State the preparation type.
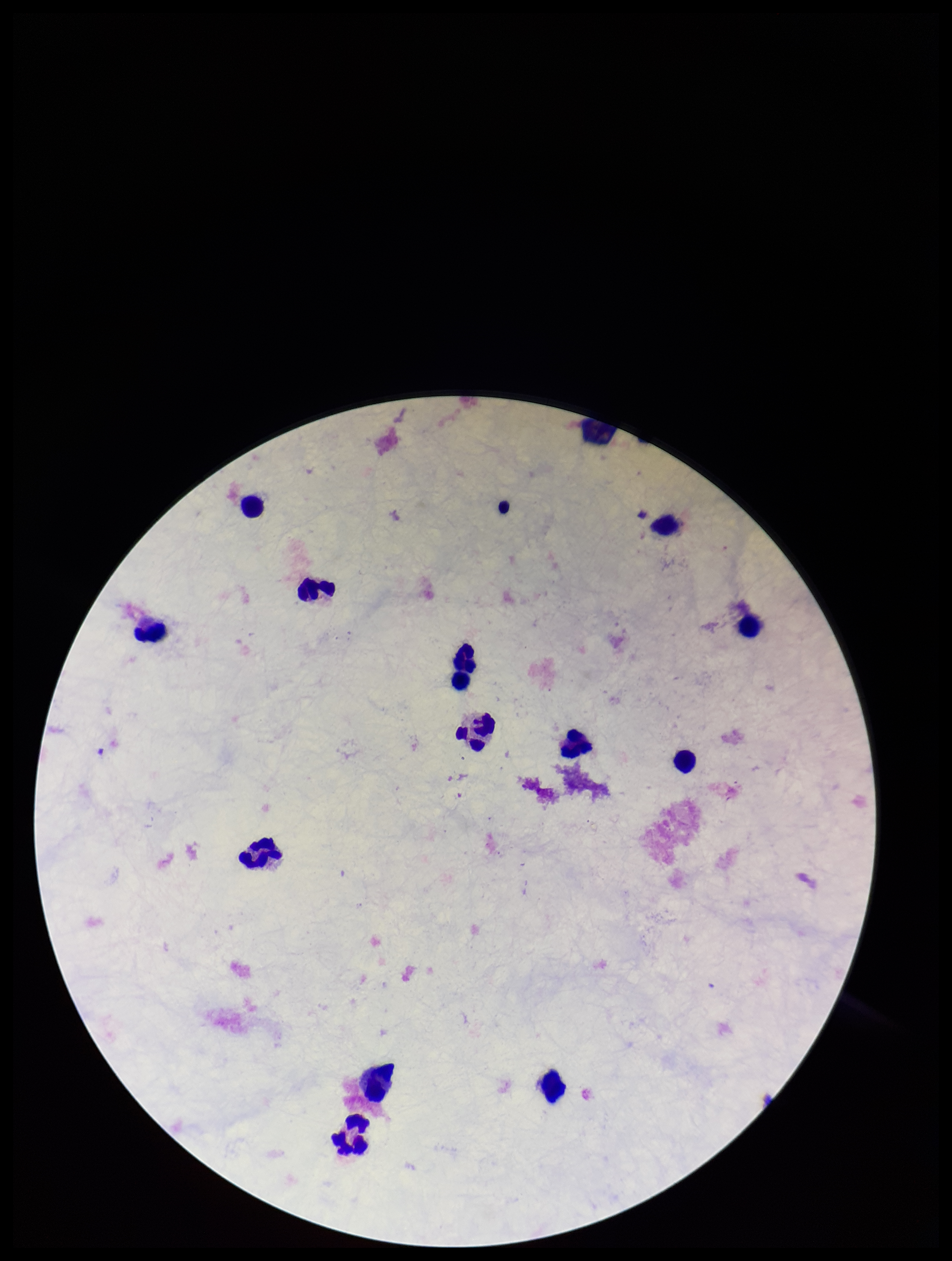

It is a thick blood smear.

Patient malaria status: negative. Parasite count: 0. Leukocyte count: 13. Stained with Giemsa. Photographed through the microscope eyepiece with a smartphone camera. One field from this slide. Plasmodium parasites: none identified. Image is 952×1261 pixels.